Locate every Plasmodium ovale-infected red blood cell.
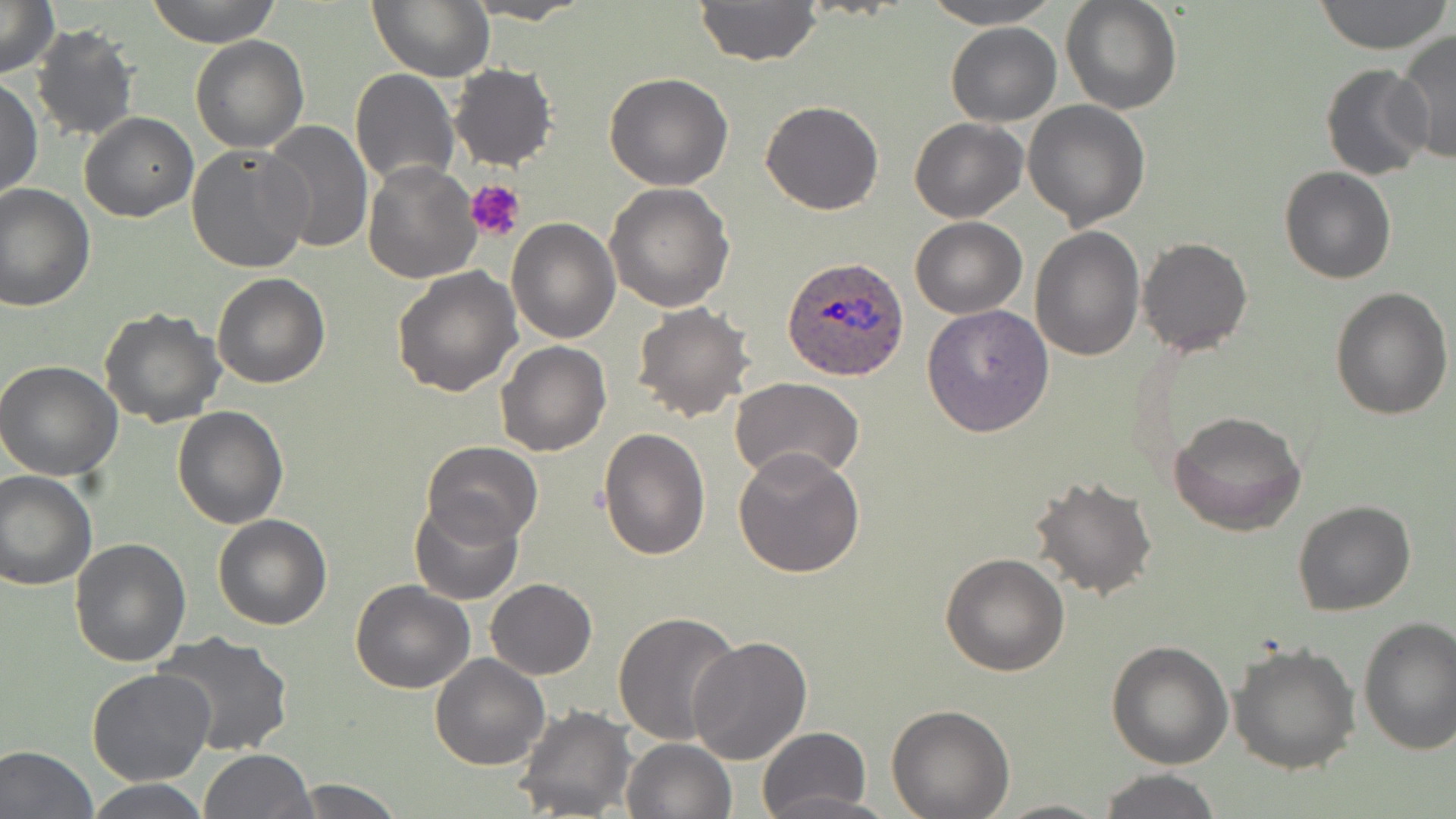

Approximate bounding boxes as [x1, y1, x2, y2] in pixels.
Plasmodium ovale-infected red blood cells: [783, 256, 911, 381].

Uninfected red blood cell locations: [0, 0, 57, 77], [147, 0, 282, 46], [367, 0, 493, 82], [694, 0, 822, 68], [919, 0, 1063, 28], [1061, 0, 1182, 113], [1311, 0, 1451, 53], [464, 1, 589, 23], [945, 22, 1063, 127], [29, 24, 140, 143], [1393, 31, 1456, 164], [191, 35, 308, 153], [45, 42, 170, 186], [449, 63, 558, 171], [1320, 63, 1431, 181], [351, 67, 458, 191], [603, 73, 732, 191], [1, 78, 43, 200], [761, 100, 883, 216], [1022, 101, 1151, 228], [79, 112, 197, 222], [909, 118, 1027, 222], [262, 122, 372, 252], [186, 141, 313, 273], [364, 159, 483, 283], [1279, 166, 1396, 284], [604, 182, 735, 314], [0, 183, 97, 311], [910, 217, 1026, 318], [506, 218, 620, 344], [1029, 225, 1145, 361], [1137, 235, 1252, 357], [392, 265, 522, 396], [211, 273, 329, 388], [1330, 285, 1453, 420], [921, 303, 1054, 436], [631, 304, 754, 424], [99, 308, 226, 427], [497, 341, 610, 456], [0, 360, 123, 480], [730, 377, 864, 485], [172, 406, 288, 529], [1170, 410, 1308, 536], [598, 426, 710, 560], [422, 440, 542, 545], [732, 446, 864, 577], [0, 470, 96, 589], [1029, 473, 1158, 601], [410, 497, 524, 606], [1293, 500, 1416, 617], [213, 513, 332, 631], [69, 537, 194, 667], [939, 552, 1070, 677], [349, 578, 475, 694], [485, 578, 597, 680], [613, 611, 742, 747], [1356, 616, 1456, 754], [154, 632, 295, 757], [688, 635, 813, 764], [1106, 640, 1234, 770], [1229, 641, 1361, 775], [429, 654, 550, 770], [87, 669, 216, 785], [887, 704, 1015, 818], [514, 705, 635, 819], [754, 727, 871, 819], [622, 737, 735, 819], [0, 745, 98, 819], [198, 749, 315, 819], [1097, 768, 1222, 819], [287, 777, 405, 819], [83, 778, 214, 817], [989, 798, 1114, 818]. Platelet locations: [467, 180, 527, 241]. Slide-level diagnosis: Plasmodium ovale. May-Grünwald-Giemsa stain. One field of a larger specimen. 1000x magnification. Thin blood smear. Light microscopy. Image is 1456×819 pixels.